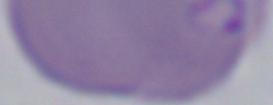
magnification = 1000x
identification = Babesia
modality = micrograph